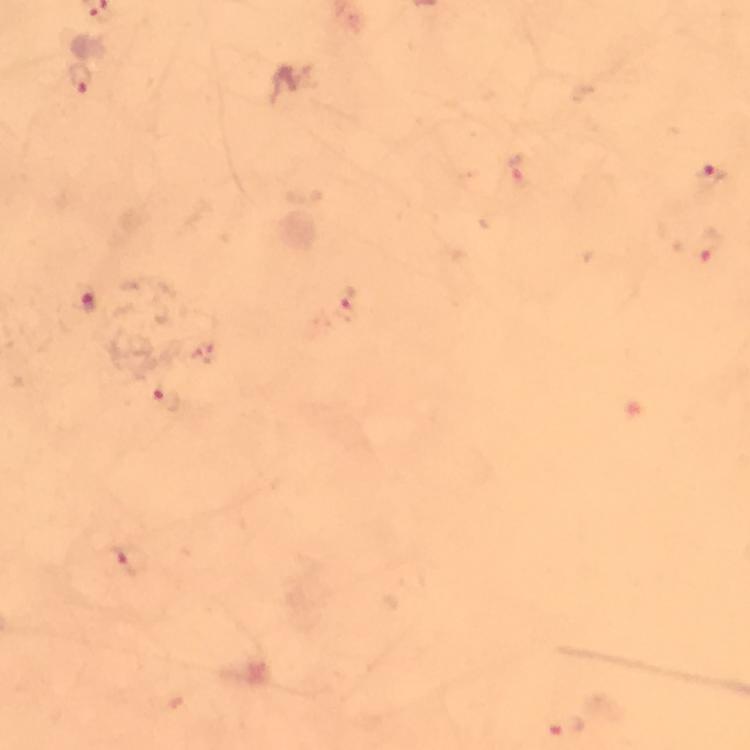

capture = smartphone photograph through a microscope
cropped from = one field of view
stain = Giemsa
preparation = thick smear
context = from a malaria diagnostic workup
immersion oil = applied
image size = 750×750 pixels
malaria parasite locations = approximate centers as (x, y) in pixels: (82, 79), (516, 170), (712, 178), (709, 246), (88, 302), (351, 305), (168, 397), (134, 561), (566, 726)
magnification = 100x